Give the position of every malaria parasite.
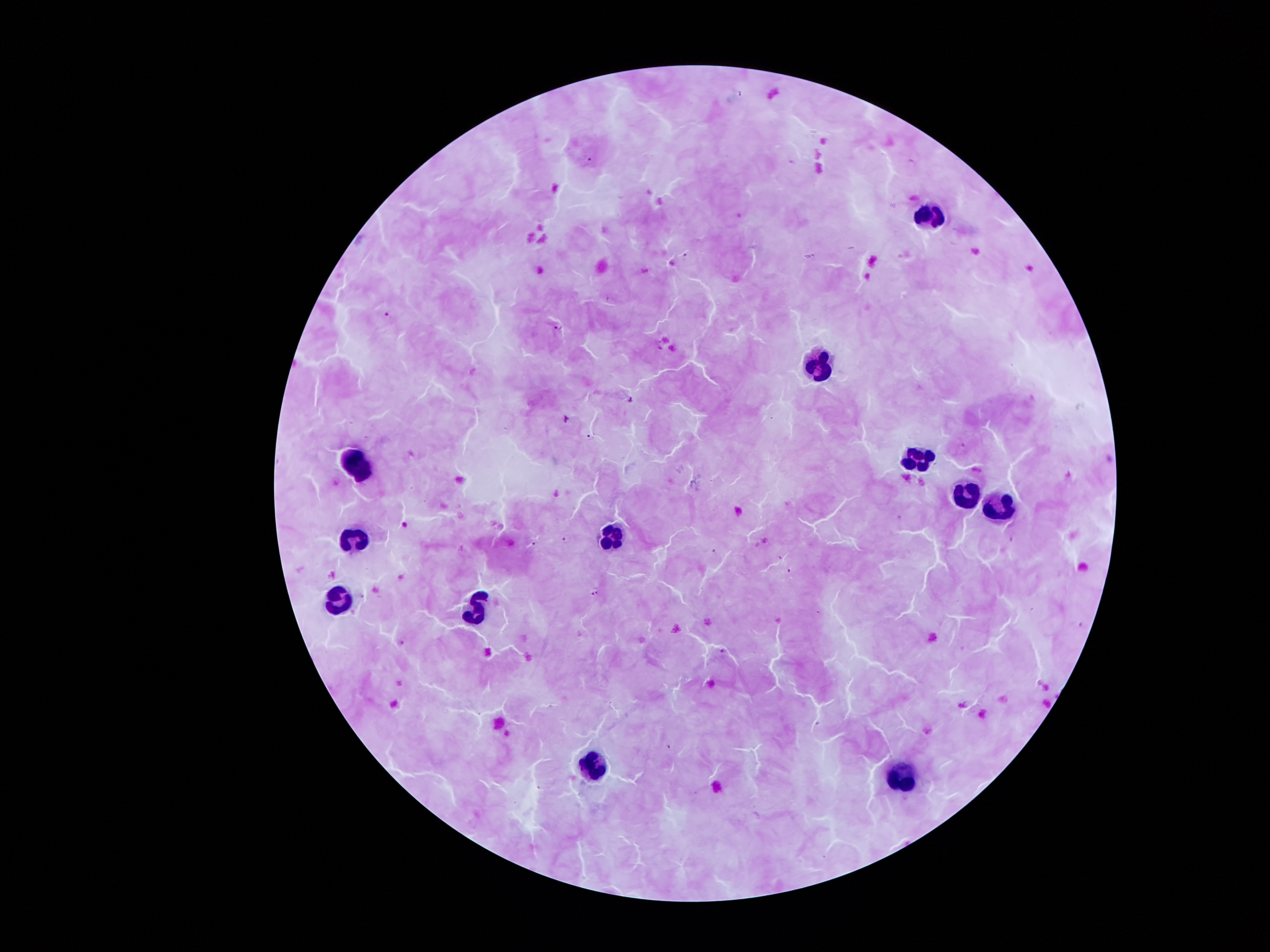

Approximate centers as {x, y} in pixels.
Malaria parasites: {589, 158}, {685, 254}, {389, 313}, {558, 328}, {591, 436}, {565, 539}, {535, 544}, {714, 550}, {788, 570}, {597, 590}, {591, 592}, {820, 614}, {722, 649}, {669, 746}.

Leukocyte locations: {930, 210}, {822, 361}, {919, 463}, {356, 468}, {965, 497}, {999, 511}, {615, 539}, {354, 546}, {340, 603}, {482, 612}, {605, 764}, {909, 774}. Thick peripheral-blood smear. Single field of view. 100x magnification. Giemsa stain. Image is 1270×952 pixels. Patient malaria status: infected with Plasmodium falciparum. Photographed through the microscope eyepiece with a smartphone camera.